Classify this cell by malaria status.
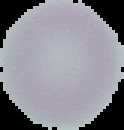

It is uninfected.

Image is 124×130 pixels. From a thin blood smear. The area outside the segmented cell region is set to black.